Classify this cell by malaria status.
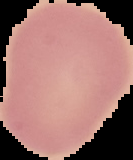
Uninfected.

Summary:
  - Preparation: thin blood smear
  - Image type: cell region segmented out of the field of view; surrounding area masked to black
  - Image size: 133×160 pixels